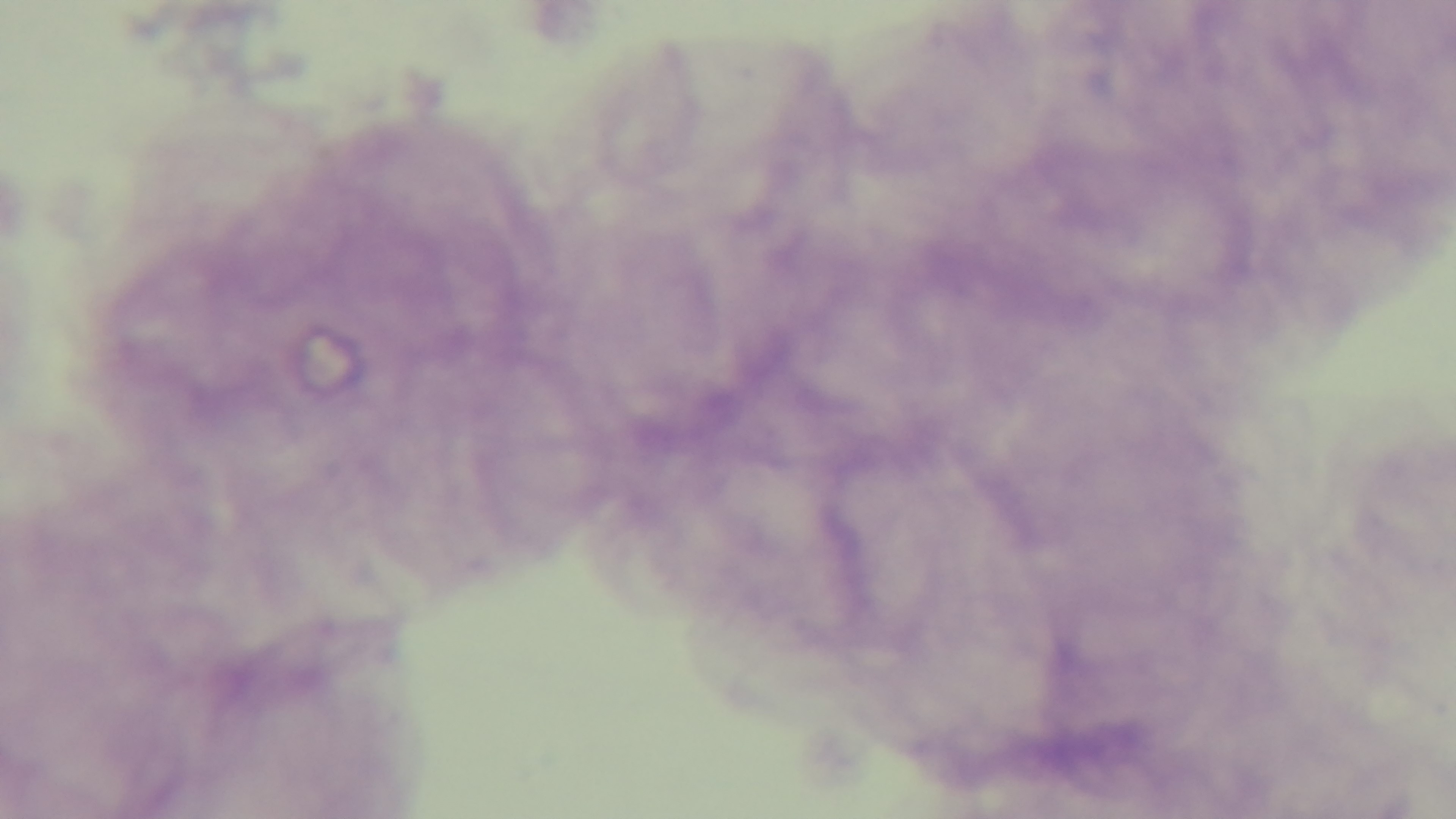
Summary:
  - Modality: light microscopy
  - Field of view: single
  - Preparation: thick smear
  - Capture: mounted 4K digital camera
  - Malaria status: uninfected
  - Objective: 100x oil immersion
  - Stain: Giemsa